Name the parasite shown.
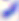
This is Toxoplasma gondii.

magnification = 400x
modality = micrograph